Assess this cell for malaria.
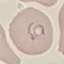
It is parasitized.

Summary:
  - Preparation: thin smear
  - Stain: Giemsa
  - Image type: automatically extracted cell patch, resized to 64 × 64 pixels
  - Capture: smartphone through the microscope eyepiece